Report the malaria status of this cell.
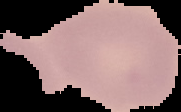
Uninfected.

Summary:
  - Preparation: thin blood smear
  - Image size: 181×112 pixels
  - Image type: cell region segmented out of the field of view; surrounding area masked to black